Assess this cell for malaria.
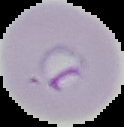
Parasitized.

Segmented cell region on a black background. Image is 124×127 pixels. From a thin blood smear.